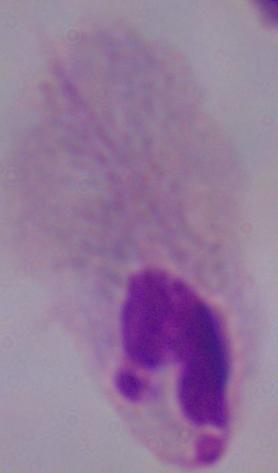

identification = trichomonad
magnification = 1000x
modality = micrograph